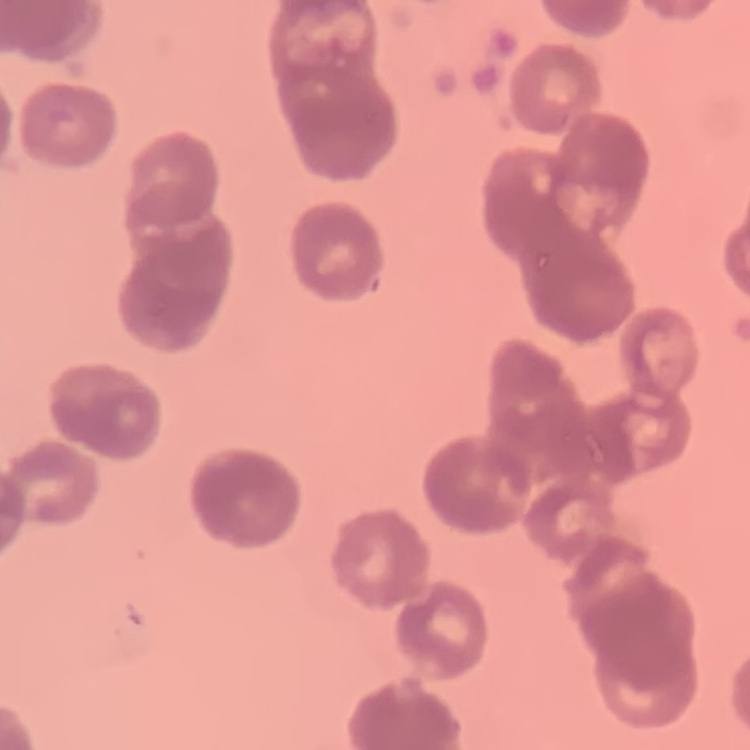
The red blood cells exhibit rouleaux formation. One tile cut from a larger photomicrograph. Thin peripheral smear. Stained with either Field's or Giemsa.